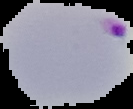 The area outside the segmented cell region is set to black. From a thin blood film. Image is 133×109 pixels. Malaria status: parasitized.